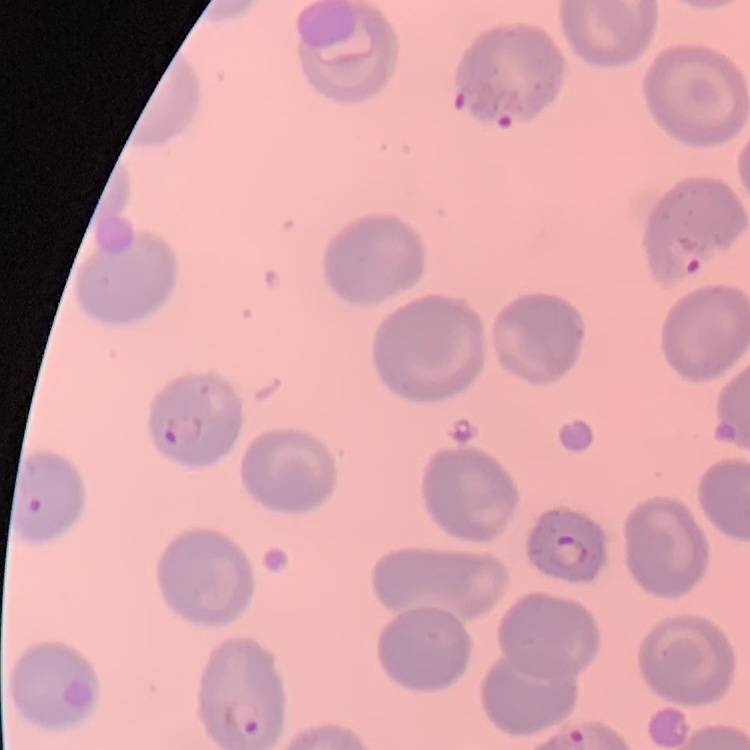
Summary:
  - Erythrocyte morphology: no rouleaux formation
  - Preparation: thin peripheral smear
  - Image type: one tile cut from a larger photomicrograph
  - Stain: Field's or Giemsa